Comment on the morphology of the erythrocytes.
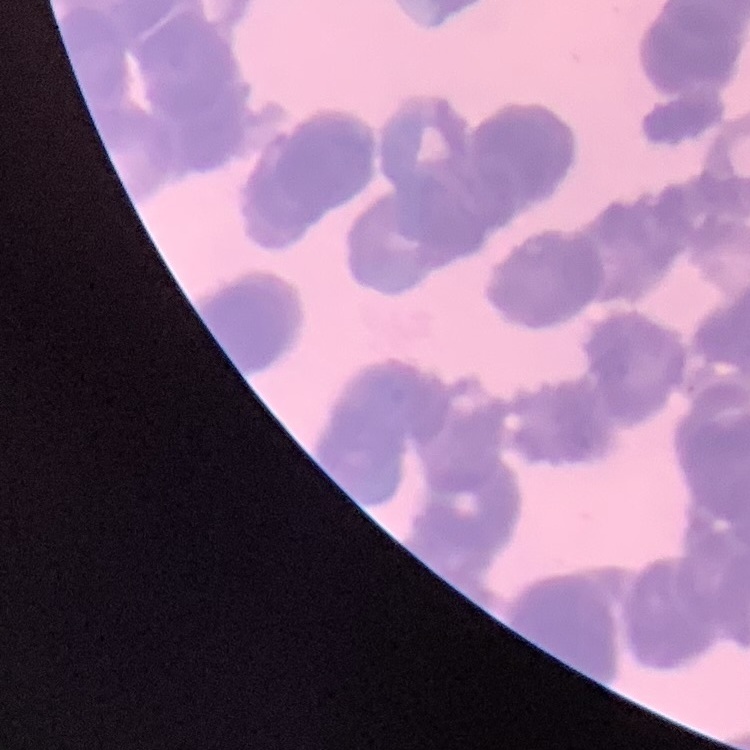
Rouleaux formation.

Summary:
  - Stain: Field's or Giemsa
  - Image type: one tile cut from a larger photomicrograph
  - Preparation: thin blood film